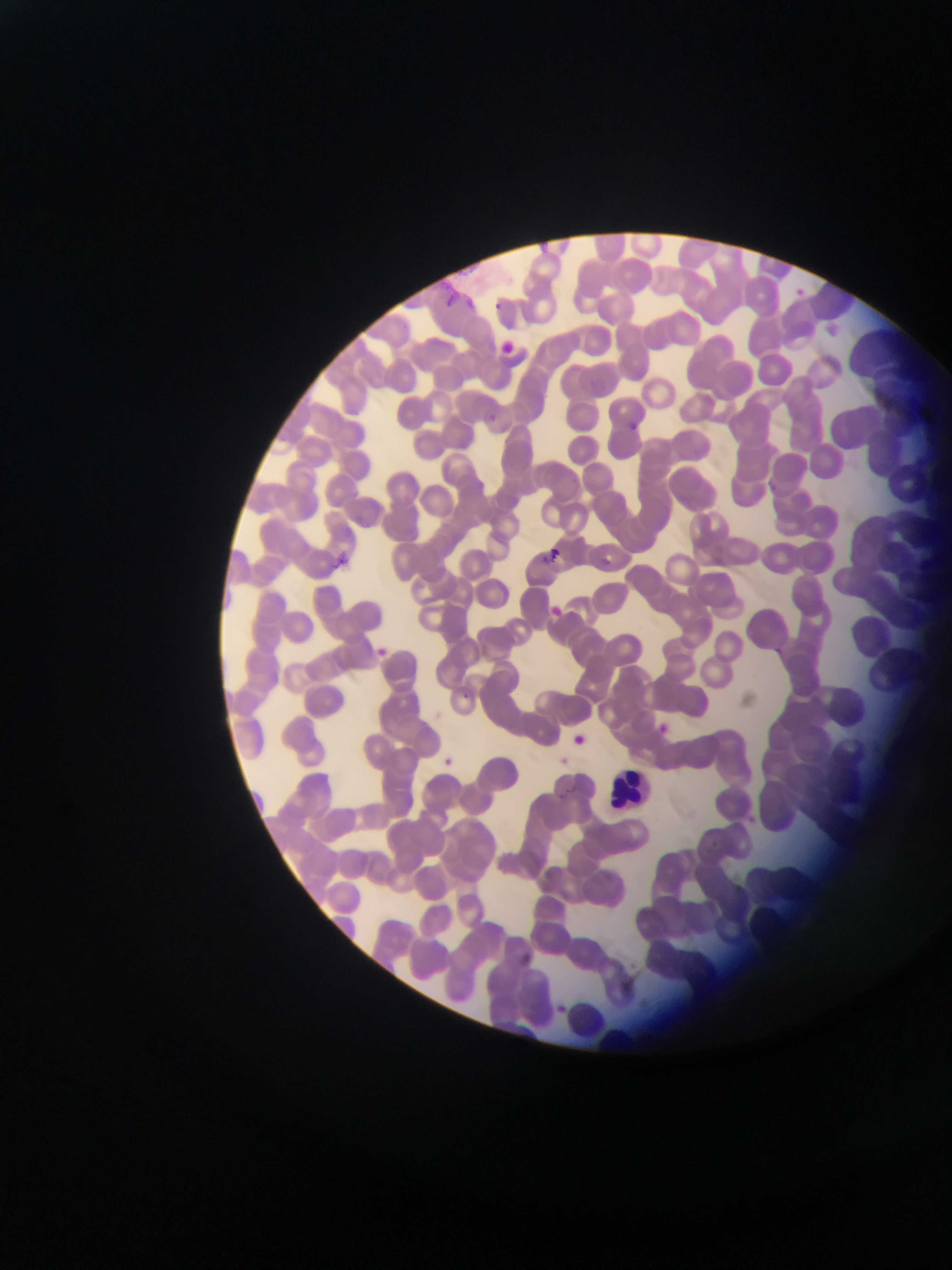

Approximate bounding boxes as left top right bottom in pixels. Leukocyte locations: 611 771 659 810. Plasmodium parasite locations: 795 277 815 307; 490 300 520 317; 488 414 499 426; 626 416 651 448; 544 542 570 560; 331 547 346 572; 549 601 571 622; 376 643 408 663; 458 688 472 705; 658 718 675 739; 572 729 596 755; 442 756 452 766; 710 837 720 850. Thin blood smear. One field of view. Collected in Ghana. Mobile-phone photograph taken through the microscope. Image is 952×1270 pixels.